Give the position of every leukocyte visible.
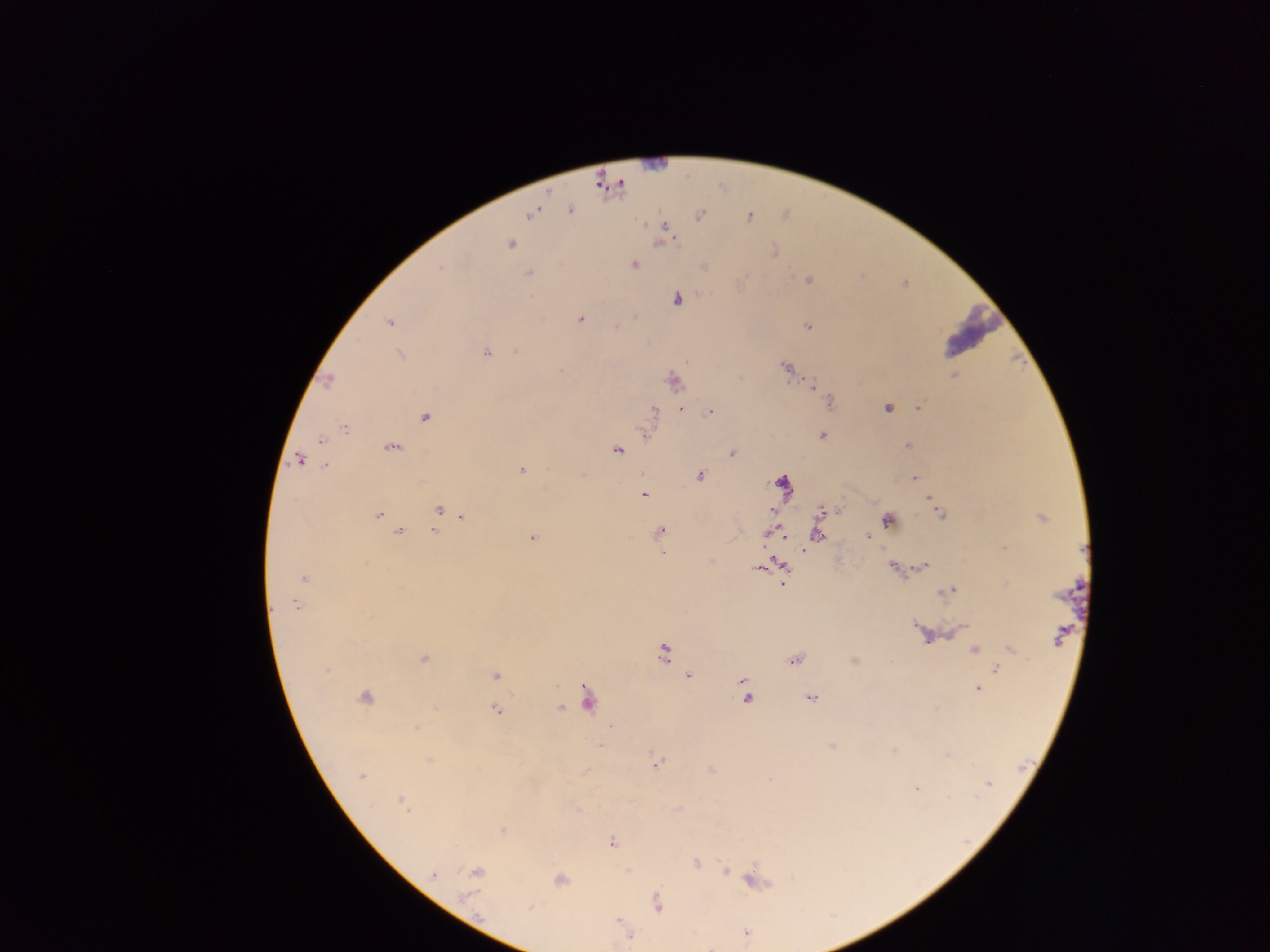
No leukocytes observed.

{
  "image_size": "1270×952 pixels",
  "capture": "mobile-phone photograph through a microscope",
  "plasmodium_parasite_locations": "approximate centers as {x, y} in pixels: {571, 210}, {531, 214}, {700, 215}, {749, 216}, {666, 228}, {510, 244}, {773, 252}, {633, 265}, {440, 268}, {528, 273}, {808, 280}, {677, 299}, {581, 319}, {389, 322}, {616, 326}, {808, 326}, {517, 351}, {487, 353}, {400, 355}, {786, 367}, {559, 370}, {954, 376}, {328, 380}, {673, 381}, {812, 385}, {829, 402}, {918, 407}, {681, 408}, {887, 408}, {654, 410}, {710, 412}, {425, 418}, {344, 428}, {821, 435}, {320, 441}, {907, 445}, {392, 447}, {617, 451}, {733, 453}, {299, 460}, {325, 465}, {522, 469}, {700, 475}, {914, 478}, {781, 482}, {644, 495}, {930, 498}, {439, 510}, {772, 510}, {838, 510}, {823, 511}, {940, 513}, {378, 515}, {462, 516}, {1041, 518}, {887, 520}, {660, 530}, {398, 531}, {433, 531}, {872, 532}, {766, 534}, {817, 534}, {868, 537}, {783, 538}, {532, 539}, {1004, 548}, {803, 550}, {662, 553}, {924, 566}, {785, 567}, {893, 567}, {757, 569}, {303, 578}, {784, 583}, {950, 590}, {296, 606}, {916, 627}, {958, 630}, {1058, 637}, {974, 649}, {1011, 649}, {663, 653}, {424, 659}, {794, 661}, {997, 669}, {326, 670}, {495, 675}, {687, 675}, {743, 682}, {745, 688}, {977, 689}, {747, 698}, {365, 699}, {587, 699}, {811, 699}, {560, 708}, {496, 710}, {415, 728}, {609, 728}, {832, 746}, {947, 754}, {429, 760}, {656, 763}, {710, 769}, {361, 776}, {987, 784}, {916, 787}, {401, 802}, {502, 831}, {612, 843}, {696, 863}, {726, 871}, {476, 873}, {433, 874}, {560, 880}, {754, 881}, {656, 902}, {530, 908}, {619, 921}, {746, 933}, {630, 937}",
  "field_of_view": "single",
  "country": "Ghana",
  "preparation": "thick blood smear"
}